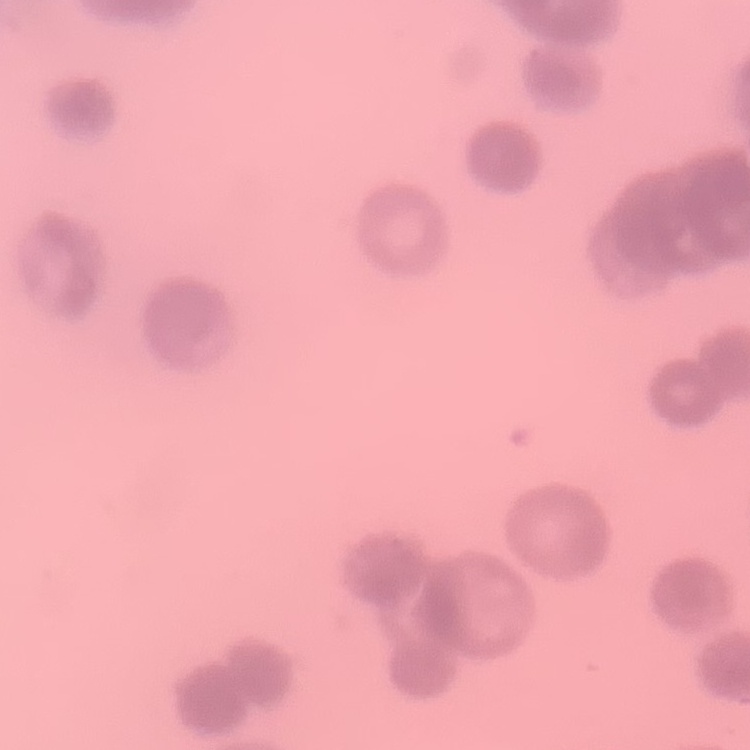

Summary:
  - Erythrocyte morphology: rouleaux formation
  - Preparation: thin blood film
  - Image type: one tile cut from a larger photomicrograph
  - Stain: Field's or Giemsa